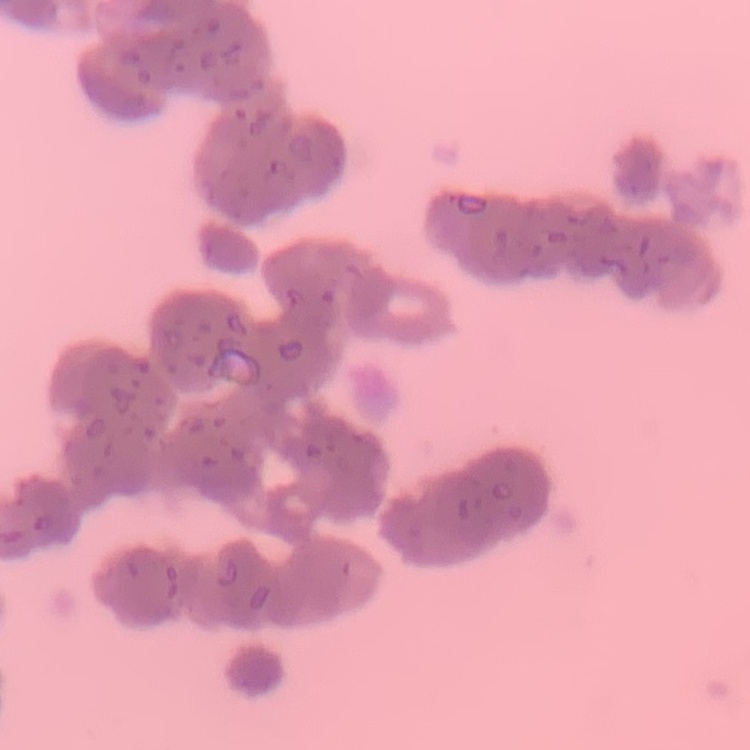

red blood cell morphology = rouleaux formation
preparation = thin blood film
image type = one tile cut from a larger photomicrograph
stain = Field's or Giemsa